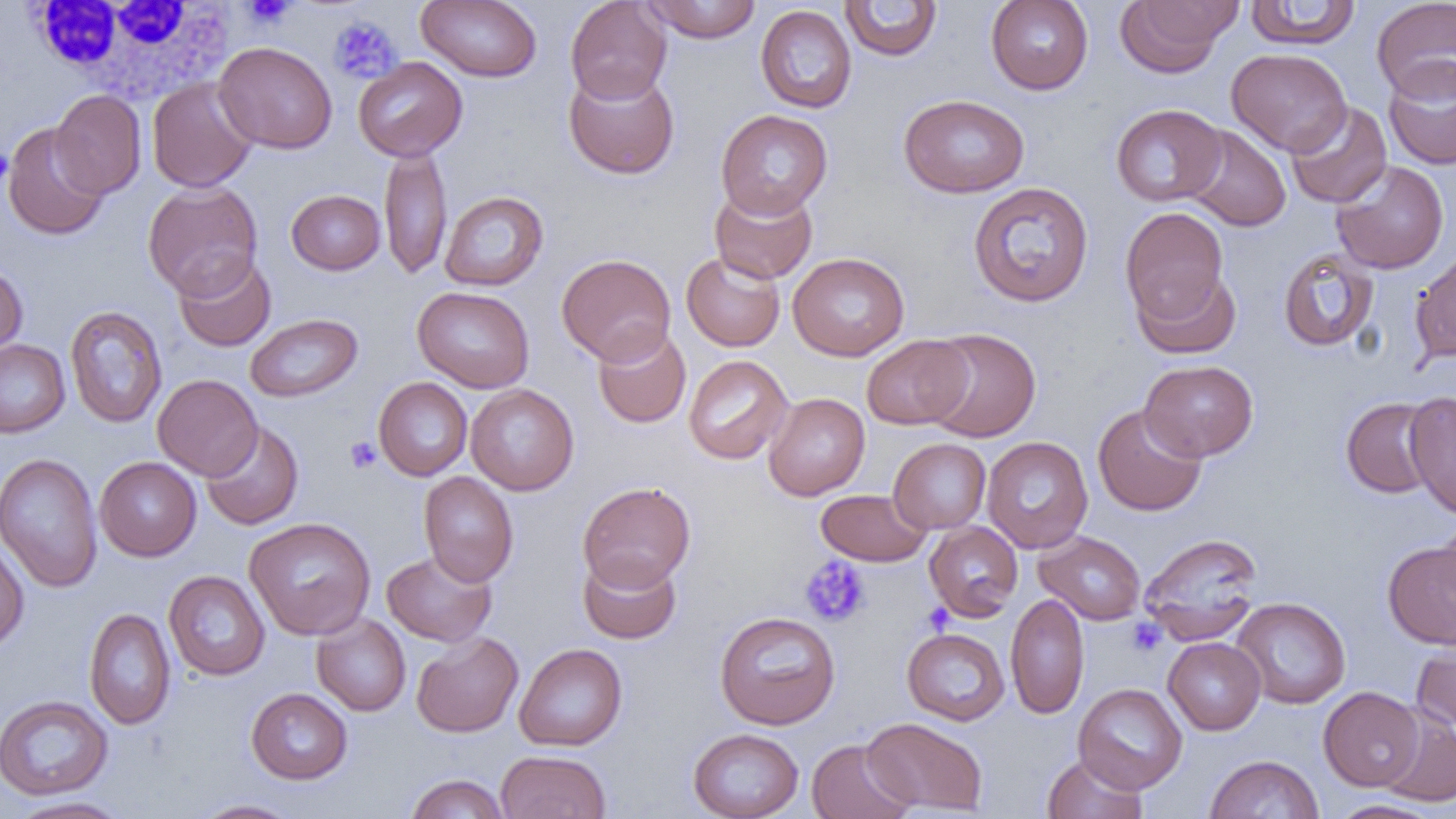
Summary:
  - Coordinate format: approximate bounding boxes as named x1/y1/x2/y2 corners in pixels
  - Uninfected red blood cell locations: (x1=416, y1=0, x2=542, y2=83), (x1=565, y1=0, x2=672, y2=104), (x1=641, y1=0, x2=763, y2=43), (x1=985, y1=0, x2=1094, y2=95), (x1=1115, y1=0, x2=1239, y2=77), (x1=1244, y1=0, x2=1362, y2=50), (x1=1371, y1=0, x2=1456, y2=101), (x1=839, y1=1, x2=943, y2=61), (x1=755, y1=5, x2=857, y2=113), (x1=214, y1=41, x2=337, y2=154), (x1=1226, y1=48, x2=1352, y2=156), (x1=353, y1=56, x2=468, y2=162), (x1=1384, y1=58, x2=1456, y2=171), (x1=563, y1=67, x2=680, y2=180), (x1=147, y1=77, x2=258, y2=193), (x1=50, y1=89, x2=147, y2=199), (x1=899, y1=94, x2=1029, y2=198), (x1=1284, y1=102, x2=1392, y2=208), (x1=1111, y1=104, x2=1226, y2=207), (x1=716, y1=109, x2=833, y2=218), (x1=2, y1=122, x2=109, y2=241), (x1=1183, y1=125, x2=1291, y2=232), (x1=379, y1=143, x2=452, y2=280), (x1=1330, y1=159, x2=1449, y2=274), (x1=142, y1=181, x2=263, y2=298), (x1=968, y1=181, x2=1094, y2=307), (x1=709, y1=184, x2=818, y2=283), (x1=286, y1=189, x2=385, y2=275), (x1=440, y1=191, x2=549, y2=291), (x1=1120, y1=207, x2=1229, y2=324), (x1=1277, y1=248, x2=1379, y2=352), (x1=1410, y1=250, x2=1456, y2=364), (x1=173, y1=252, x2=276, y2=352), (x1=681, y1=252, x2=785, y2=352), (x1=788, y1=252, x2=910, y2=360), (x1=556, y1=253, x2=676, y2=365), (x1=0, y1=262, x2=28, y2=360), (x1=1133, y1=268, x2=1242, y2=360), (x1=412, y1=286, x2=535, y2=393), (x1=65, y1=305, x2=167, y2=428), (x1=245, y1=313, x2=363, y2=402), (x1=592, y1=324, x2=691, y2=429), (x1=921, y1=327, x2=1042, y2=443), (x1=861, y1=335, x2=973, y2=430), (x1=0, y1=338, x2=70, y2=437), (x1=684, y1=355, x2=793, y2=464), (x1=1139, y1=360, x2=1258, y2=462), (x1=153, y1=374, x2=262, y2=481), (x1=373, y1=377, x2=472, y2=481), (x1=465, y1=384, x2=579, y2=496), (x1=1403, y1=391, x2=1456, y2=519), (x1=763, y1=392, x2=870, y2=500), (x1=1341, y1=397, x2=1441, y2=498), (x1=1092, y1=404, x2=1207, y2=517), (x1=200, y1=421, x2=304, y2=530), (x1=981, y1=436, x2=1093, y2=553), (x1=888, y1=438, x2=991, y2=534), (x1=0, y1=452, x2=104, y2=593), (x1=95, y1=457, x2=202, y2=561), (x1=418, y1=471, x2=518, y2=587), (x1=578, y1=481, x2=696, y2=591), (x1=816, y1=489, x2=931, y2=566), (x1=244, y1=516, x2=375, y2=640), (x1=1434, y1=516, x2=1456, y2=619), (x1=924, y1=522, x2=1023, y2=621), (x1=1033, y1=530, x2=1146, y2=625), (x1=1139, y1=532, x2=1263, y2=643), (x1=0, y1=540, x2=29, y2=652), (x1=1382, y1=541, x2=1456, y2=649), (x1=381, y1=549, x2=497, y2=647), (x1=577, y1=552, x2=682, y2=644), (x1=164, y1=570, x2=270, y2=680), (x1=1005, y1=592, x2=1089, y2=719), (x1=1230, y1=597, x2=1351, y2=709), (x1=84, y1=607, x2=176, y2=729), (x1=714, y1=611, x2=840, y2=729), (x1=311, y1=613, x2=411, y2=716), (x1=308, y1=619, x2=522, y2=721), (x1=902, y1=627, x2=1010, y2=725), (x1=411, y1=632, x2=523, y2=737), (x1=1163, y1=637, x2=1266, y2=735), (x1=1411, y1=640, x2=1456, y2=735), (x1=514, y1=642, x2=628, y2=751), (x1=1073, y1=682, x2=1188, y2=794), (x1=1318, y1=686, x2=1424, y2=791), (x1=246, y1=688, x2=353, y2=784), (x1=0, y1=694, x2=113, y2=801), (x1=1377, y1=708, x2=1456, y2=808), (x1=862, y1=717, x2=988, y2=815), (x1=688, y1=728, x2=804, y2=818), (x1=806, y1=739, x2=914, y2=819), (x1=496, y1=750, x2=611, y2=819), (x1=1041, y1=753, x2=1147, y2=818), (x1=1205, y1=754, x2=1324, y2=818), (x1=405, y1=773, x2=510, y2=818), (x1=8, y1=796, x2=132, y2=819), (x1=192, y1=799, x2=300, y2=818), (x1=1327, y1=799, x2=1446, y2=818)
  - White blood cell locations: (x1=23, y1=0, x2=239, y2=102)
  - Platelet locations: (x1=242, y1=0, x2=296, y2=28), (x1=328, y1=15, x2=402, y2=83), (x1=0, y1=147, x2=13, y2=188), (x1=344, y1=436, x2=381, y2=473), (x1=799, y1=555, x2=870, y2=627), (x1=922, y1=603, x2=955, y2=635), (x1=1126, y1=618, x2=1166, y2=656)
  - Slide-level diagnosis: negative for blood parasites
  - Field of view: one of a larger specimen
  - Preparation: thin blood smear
  - Image size: 1456×819 pixels
  - Modality: light microscopy
  - Magnification: 1000x